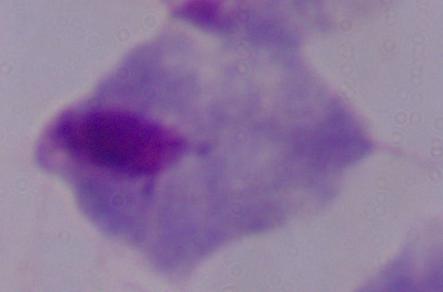

Summary:
  - Identification: trichomonad
  - Magnification: 1000x
  - Modality: photomicrograph